Report the malaria status of this cell.
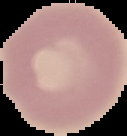
Uninfected.

Image is 127×136 pixels. Cell region segmented out of the field of view; the surrounding area is masked to black. From a thin blood smear.